Outline each Plasmodium falciparum-infected red blood cell.
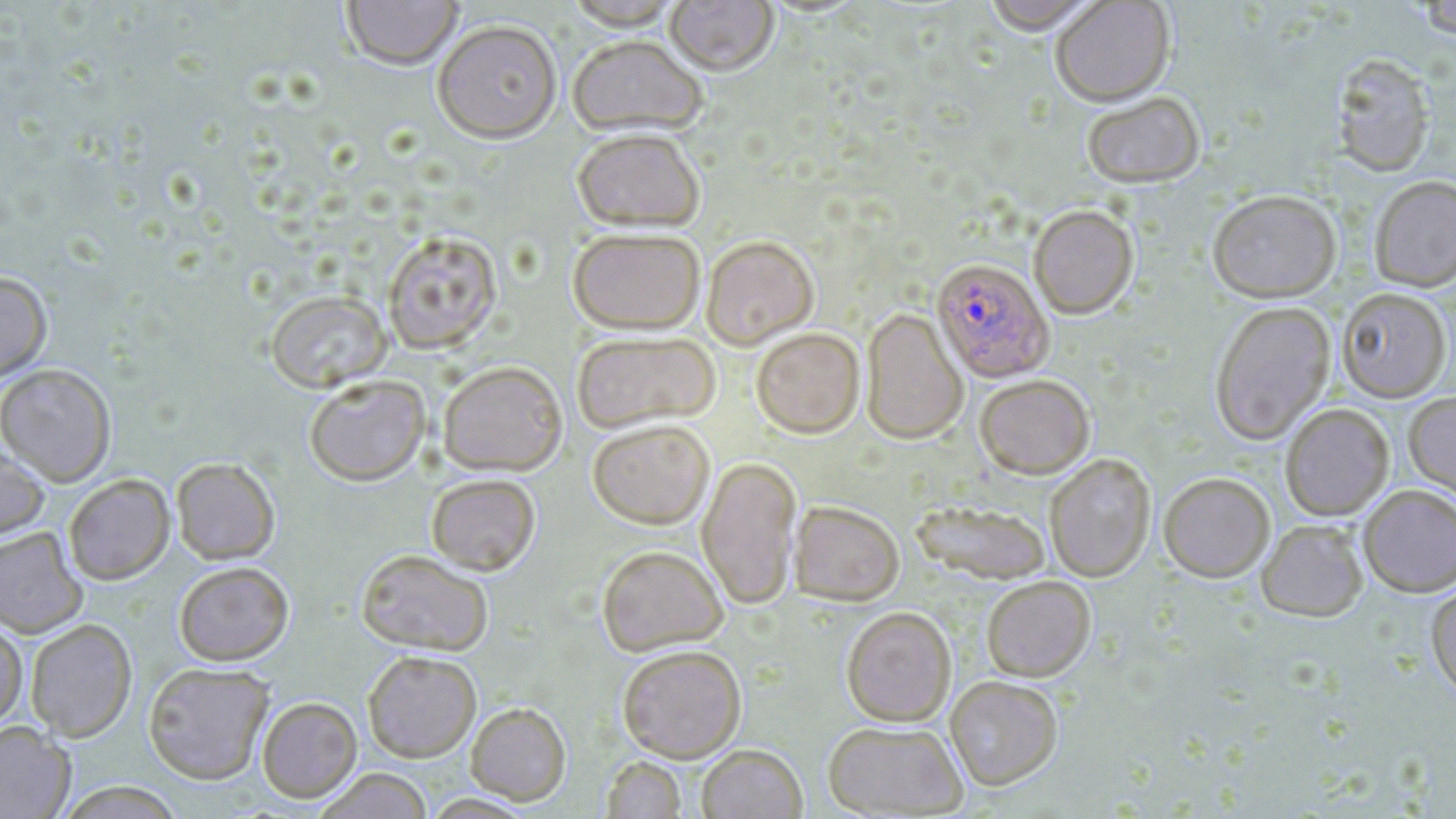

Approximate bounding boxes as (x1,y1)-(x2,y2) corner pairs in pixels.
Plasmodium falciparum-infected red blood cells: (931,259)-(1054,383).

Summary:
  - Uninfected red blood cell locations: (341,0)-(463,72), (665,0)-(779,79), (981,0)-(1104,38), (563,1)-(684,34), (1051,1)-(1176,110), (1413,1)-(1456,41), (432,23)-(563,145), (567,38)-(707,140), (1330,54)-(1437,178), (1083,94)-(1205,191), (572,132)-(705,234), (1369,176)-(1456,293), (1207,192)-(1341,303), (1029,206)-(1139,320), (568,229)-(705,336), (383,231)-(502,353), (700,237)-(820,351), (0,271)-(52,382), (1337,288)-(1452,403), (266,289)-(392,393), (1209,302)-(1336,446), (861,309)-(968,445), (751,328)-(865,439), (571,331)-(721,434), (437,360)-(568,475), (0,363)-(117,486), (303,374)-(431,486), (975,377)-(1095,480), (1404,391)-(1456,507), (1280,404)-(1395,522), (586,419)-(716,530), (0,443)-(50,541), (1045,453)-(1156,583), (697,456)-(803,611), (171,457)-(280,564), (426,473)-(541,575), (63,474)-(175,585), (1159,474)-(1275,584), (1358,485)-(1456,597), (789,500)-(905,606), (910,500)-(1051,585), (1256,520)-(1368,623), (0,527)-(88,638), (597,545)-(728,655), (356,549)-(494,656), (173,561)-(294,665), (981,577)-(1096,682), (1426,583)-(1456,702), (841,606)-(957,726), (26,618)-(137,742), (0,619)-(28,730), (616,644)-(747,762), (362,649)-(482,762), (143,661)-(274,785), (945,676)-(1063,791), (256,696)-(362,802), (466,702)-(571,805), (823,720)-(968,817), (0,721)-(75,819), (697,743)-(807,819), (601,756)-(687,818), (313,768)-(433,818), (58,782)-(186,819)
  - Slide-level diagnosis: Plasmodium falciparum
  - Stain: May-Grünwald-Giemsa
  - Field of view: one of a larger specimen
  - Modality: optical microscopy
  - Magnification: 1000x
  - Image size: 1456×819 pixels
  - Preparation: thin blood film